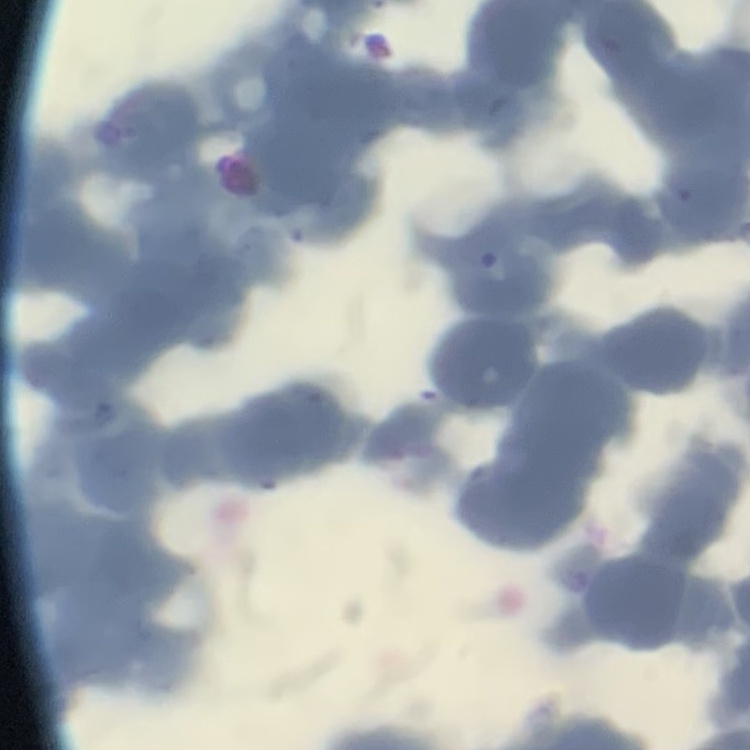
The red blood cells exhibit rouleaux formation. Field's or Giemsa stain. Thin blood smear. Square crop of a larger photomicrograph.